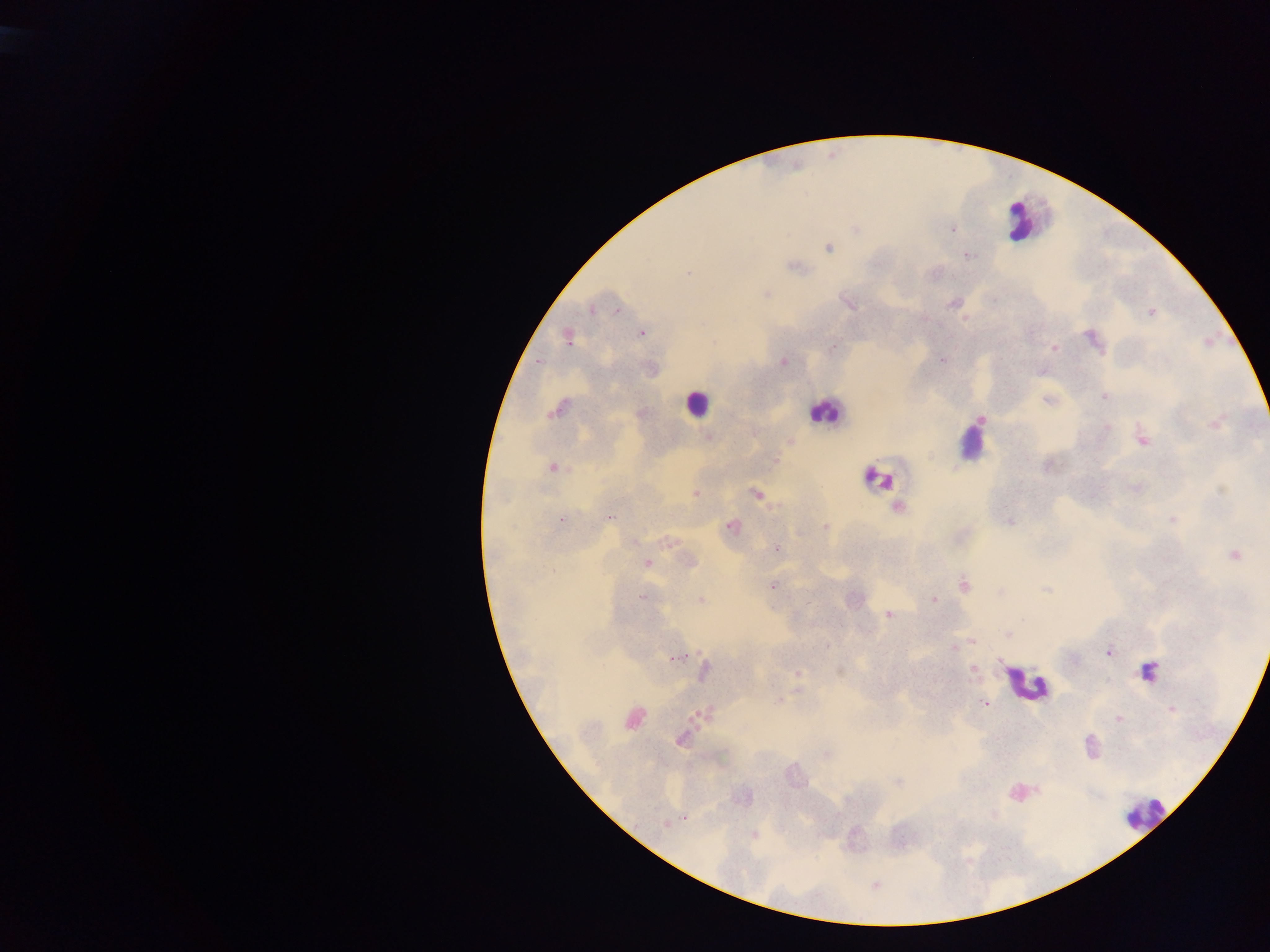
Approximate centers as x y in pixels. Leukocyte locations: 1022 220; 696 403; 825 411; 973 438; 878 477; 1148 671; 1026 684; 1021 792; 1144 813. Malaria parasite locations: 855 227; 827 247; 966 255; 792 266; 687 272; 766 294; 847 303; 954 303; 592 309; 617 311; 1151 312; 964 319; 641 332; 567 336; 1093 340; 832 348; 1053 348; 941 359; 539 361; 782 361; 1042 371; 1104 397; 1048 399; 558 409; 980 418; 1215 422; 1106 426; 709 437; 1141 438; 788 440; 772 460; 551 467; 1136 488; 695 494; 756 494; 897 507; 608 517; 1172 518; 559 519; 1009 521; 731 526; 825 527; 671 540; 776 550; 1234 555; 689 561; 646 563; 964 584; 772 585; 1045 589; 1001 592; 642 596; 700 599; 932 599; 889 614; 1007 633; 972 641; 827 646; 954 646; 1107 652; 677 657; 973 669; 704 671; 838 671; 797 673; 779 700; 984 703; 1171 709; 704 714; 1118 718; 632 719; 680 739; 826 754; 899 782; 685 817; 667 823; 753 834; 875 884. Collected in Ghana. One field of view. Photographed through a microscope with a mobile-phone camera. Image is 1270×952 pixels. Thick blood smear.